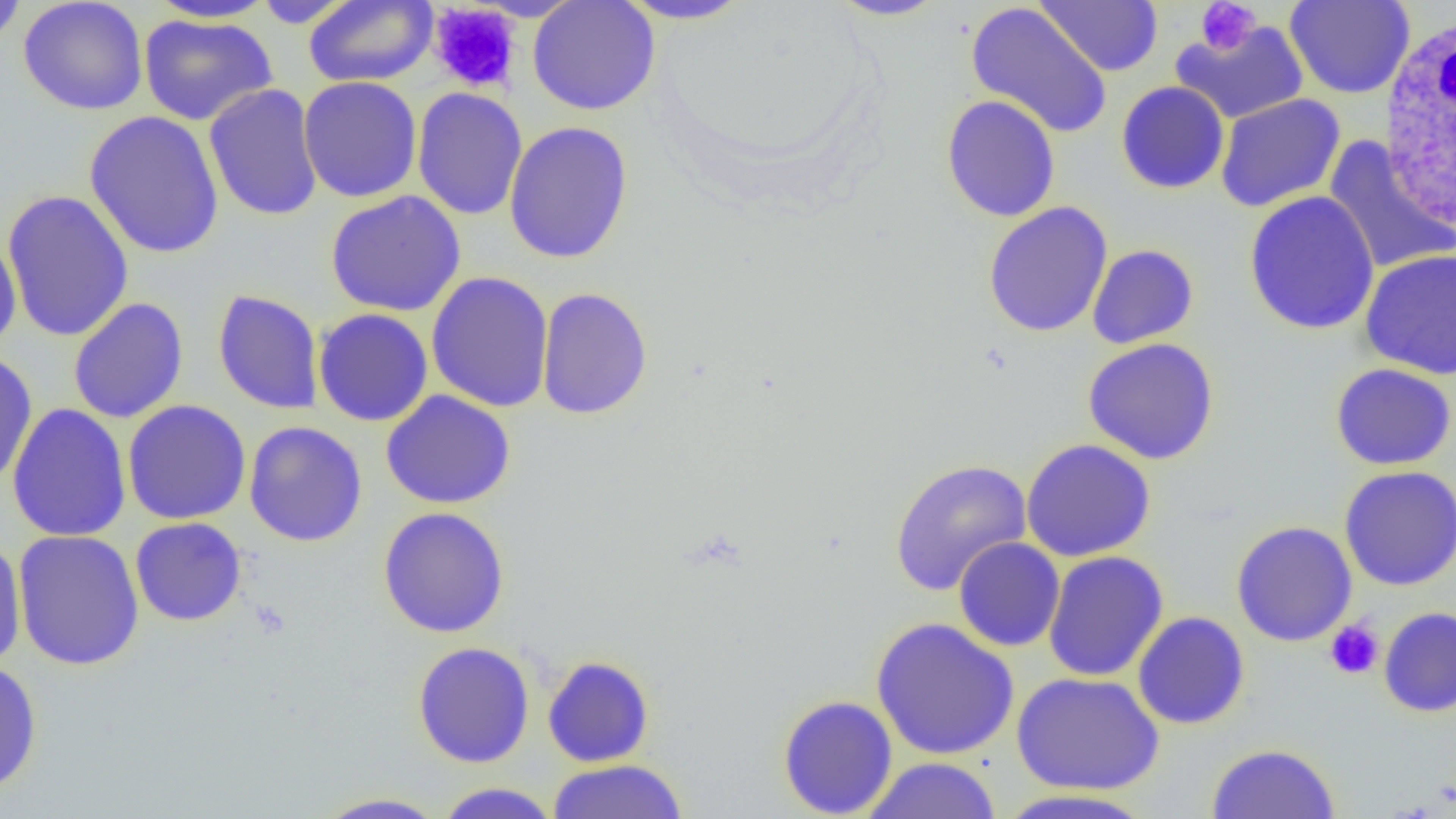 Approximate bounding boxes as [x1, y1, x2, y2] in pixels. White blood cell locations: [1378, 12, 1456, 235]. Platelet locations: [1196, 1, 1261, 55], [428, 3, 523, 94], [1324, 619, 1385, 679]. Uninfected red blood cell locations: [18, 0, 148, 116], [528, 0, 660, 115], [616, 0, 755, 24], [829, 0, 949, 21], [1036, 0, 1163, 76], [1284, 0, 1415, 99], [0, 1, 27, 48], [144, 1, 280, 23], [251, 1, 360, 28], [303, 1, 438, 87], [966, 2, 1113, 140], [138, 13, 277, 126], [1171, 20, 1308, 124], [298, 76, 422, 203], [1116, 81, 1230, 194], [204, 83, 322, 222], [411, 86, 528, 221], [1215, 93, 1345, 212], [940, 94, 1060, 222], [84, 109, 224, 259], [503, 120, 634, 265], [1323, 136, 1455, 275], [2, 189, 135, 343], [1243, 190, 1380, 335], [325, 191, 466, 317], [982, 201, 1113, 338], [0, 231, 22, 358], [1087, 244, 1199, 348], [1360, 249, 1456, 380], [425, 271, 554, 413], [536, 286, 653, 421], [212, 289, 326, 415], [68, 297, 189, 424], [313, 307, 433, 426], [1082, 337, 1220, 464], [0, 350, 38, 490], [1330, 362, 1456, 470], [380, 390, 516, 509], [122, 400, 251, 525], [7, 403, 132, 543], [243, 420, 368, 547], [1021, 438, 1156, 562], [889, 457, 1033, 596], [1339, 465, 1456, 591], [377, 506, 511, 638], [130, 517, 247, 627], [1231, 520, 1358, 647], [12, 529, 145, 671], [953, 537, 1065, 652], [0, 538, 27, 671], [1043, 551, 1169, 682], [1378, 606, 1456, 717], [1132, 612, 1250, 730], [870, 616, 1020, 761], [412, 641, 535, 768], [542, 655, 654, 767], [0, 659, 43, 796], [1011, 671, 1164, 795], [777, 694, 898, 818], [1205, 742, 1341, 819], [860, 756, 1002, 818], [546, 759, 689, 818], [433, 782, 562, 818], [995, 788, 1159, 817], [312, 792, 450, 818]. Slide-level diagnosis: no evidence of blood parasites. Image is 1456×819 pixels. One field of a larger specimen. Captured at 1000x magnification. Thin blood film. Light microscopy.